Report the malaria status of this cell.
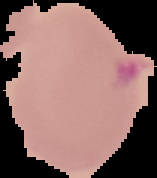

It is parasitized.

Image is 157×178 pixels. Segmented cell region on a black background. From a thin blood smear.